Describe the morphology of the red blood cells.
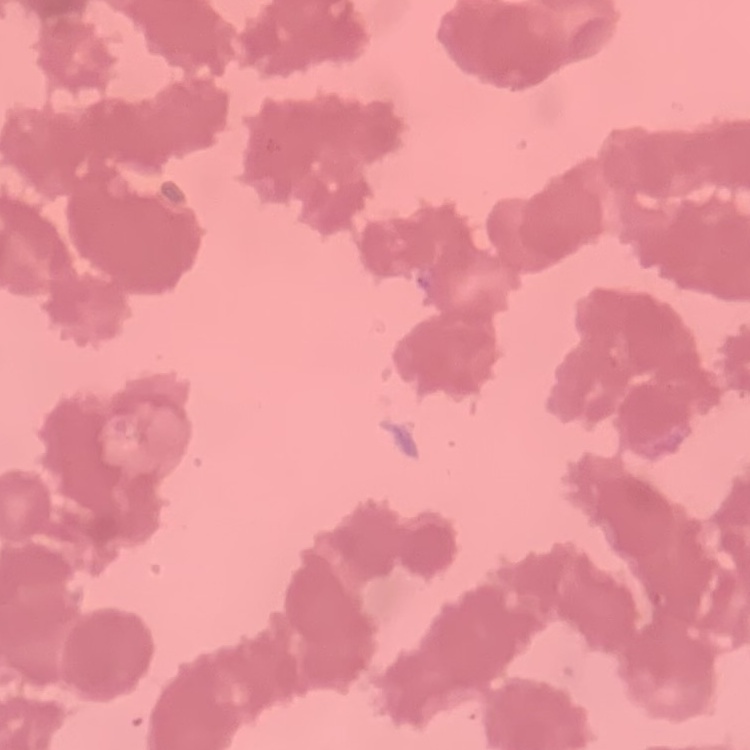
Rouleaux formation.

Stained with either Field's or Giemsa. Thin blood film. One tile cut from a larger photomicrograph.